Assess this cell for malaria.
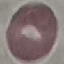

It is uninfected.

Summary:
  - Stain: Giemsa
  - Image type: cell patch, automatically extracted from a larger field of view and resized to 64 × 64 pixels
  - Capture: smartphone camera at the microscope eyepiece
  - Preparation: thin blood smear